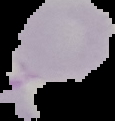

malaria status = uninfected
image size = 115×121 pixels
preparation = thin blood smear
image type = segmented cell region with the area outside set to black